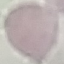
Result: negative for malaria parasites. Thin blood smear. Giemsa-stained preparation. Cell patch, automatically extracted from a larger field of view and resized to 64 × 64 pixels. Photographed with a smartphone camera at the microscope eyepiece.